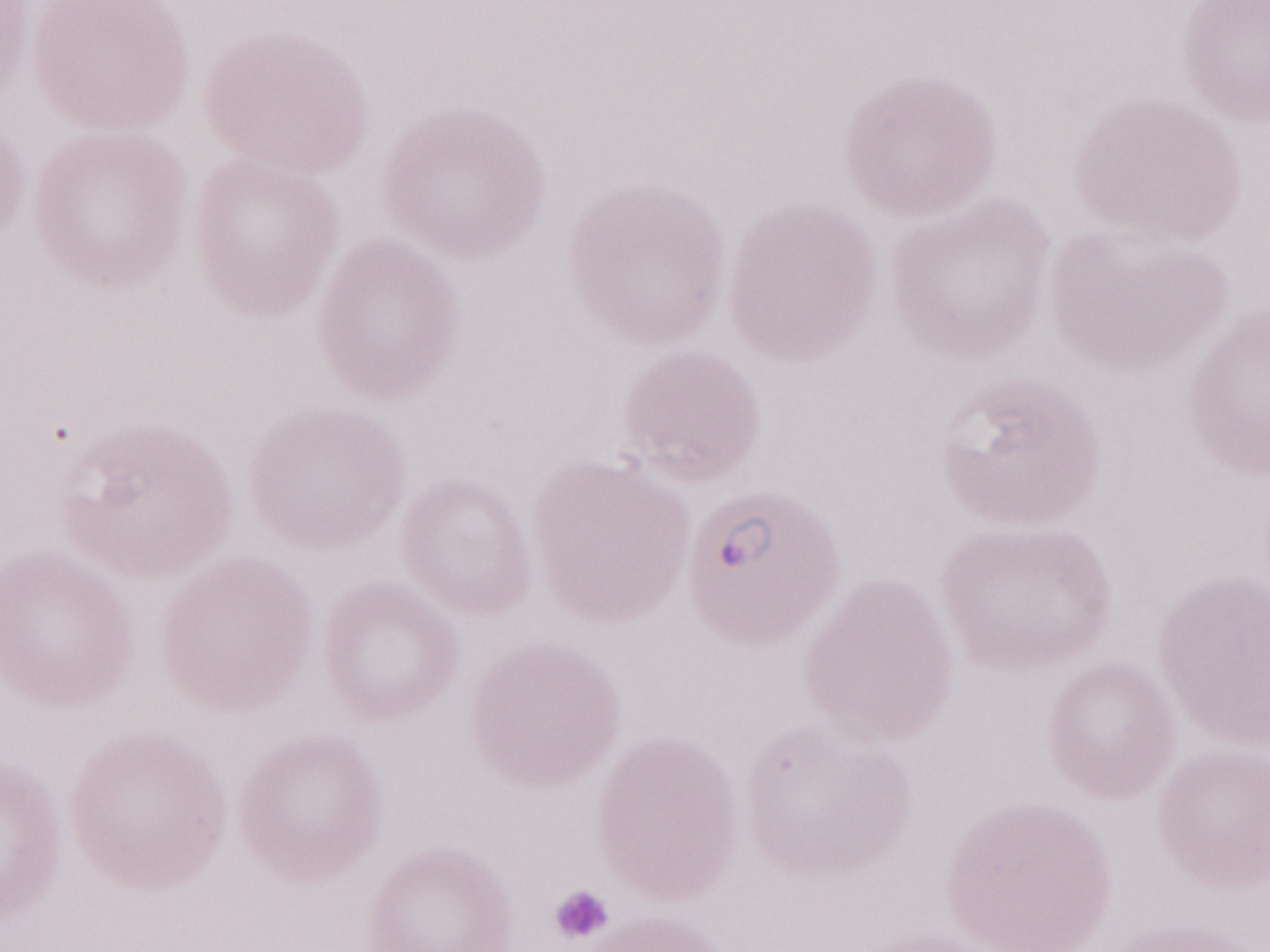

Olympus BX43 microscope, Olympus DP73 camera. Single field of view. 1,000x magnification. Image is 1270×952 pixels. Thin blood smear. Patient-level malaria diagnosis: positive. May-Grünwald-Giemsa (MGG) stain.